Name the cell type shown.
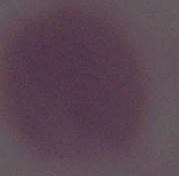

An erythrocyte.

Summary:
  - Modality: photomicrograph
  - Magnification: 1000x